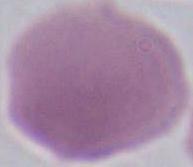 Micrograph. 1000x magnification. A red blood cell is shown.